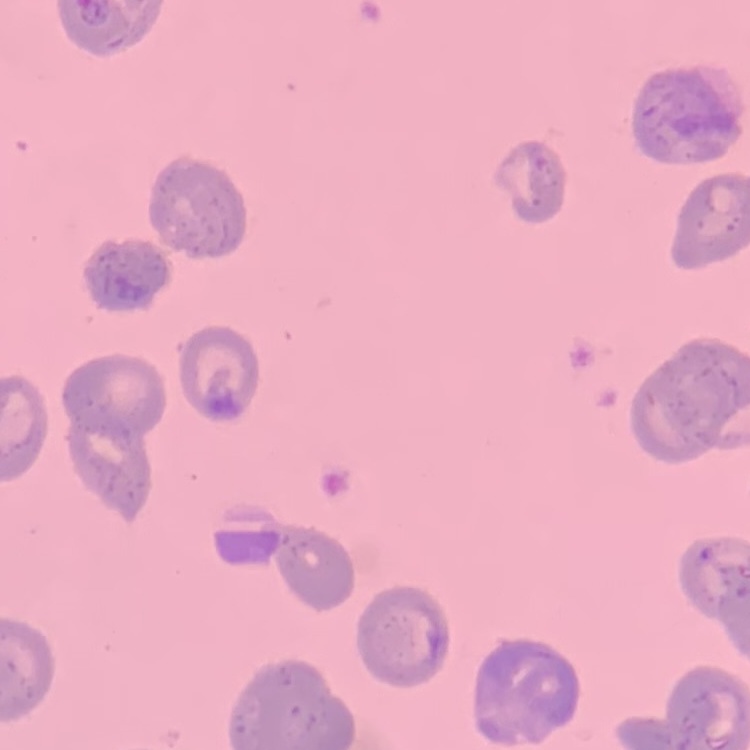

The erythrocytes show no rouleaux formation. One tile cut from a larger photomicrograph. Thin peripheral smear. Field's or Giemsa stain.